Locate every Plasmodium falciparum-infected red blood cell.
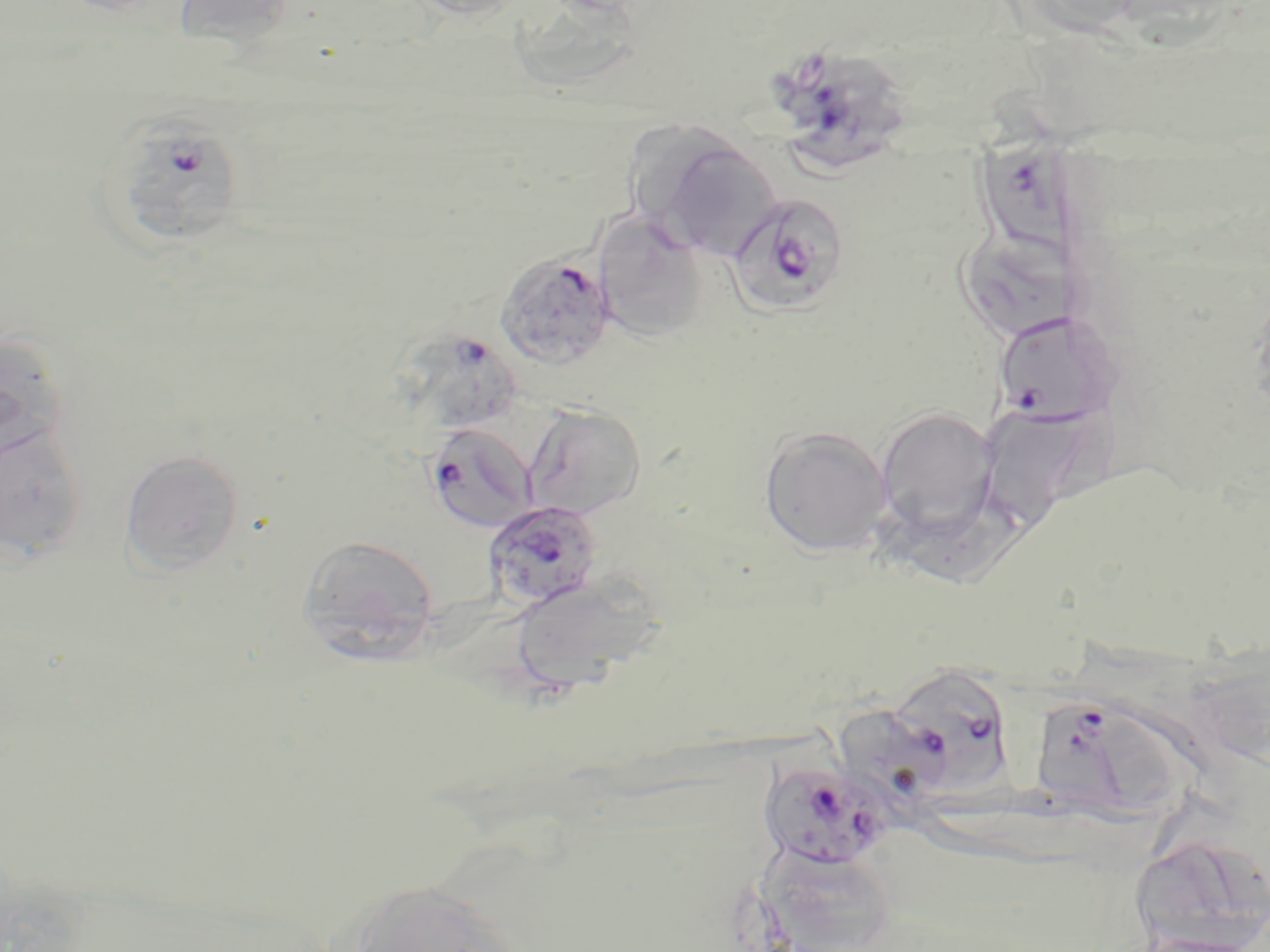

Approximate bounding boxes as [x1, y1, x2, y2] in pixels.
Plasmodium falciparum-infected red blood cells: [786, 59, 913, 178], [972, 110, 1078, 251], [94, 112, 249, 253], [725, 188, 849, 317], [494, 251, 618, 370], [992, 318, 1122, 428], [407, 328, 524, 429], [425, 422, 538, 533], [483, 501, 602, 610], [906, 671, 1011, 800], [1038, 698, 1184, 834], [835, 702, 964, 823], [760, 760, 891, 870].

slide_level_diagnosis: Plasmodium falciparum
modality: light microscopy
stain: May-Grünwald-Giemsa
field_of_view: single
magnification: 1000x
uninfected_red_blood_cell_locations: 'approximate bounding boxes as [x1, y1, x2, y2] in pixels: [170, 0, 297, 47], [405, 0, 529, 21], [516, 0, 640, 95], [635, 128, 783, 261], [593, 212, 709, 342], [965, 225, 1082, 341], [0, 331, 68, 476], [522, 403, 647, 520], [984, 403, 1093, 529], [875, 406, 999, 540], [0, 421, 88, 564], [758, 425, 892, 556], [120, 448, 245, 576], [882, 489, 1031, 592], [296, 534, 439, 660], [510, 575, 664, 694], [1138, 847, 1248, 952], [336, 878, 534, 952]'
preparation: thin blood smear
image_size: 1270×952 pixels